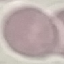

Summary:
  - Result: negative for malaria parasites
  - Preparation: thin blood film
  - Stain: Giemsa
  - Capture: smartphone through the microscope eyepiece
  - Image type: cell patch, automatically extracted from a larger field of view and resized to 64 × 64 pixels